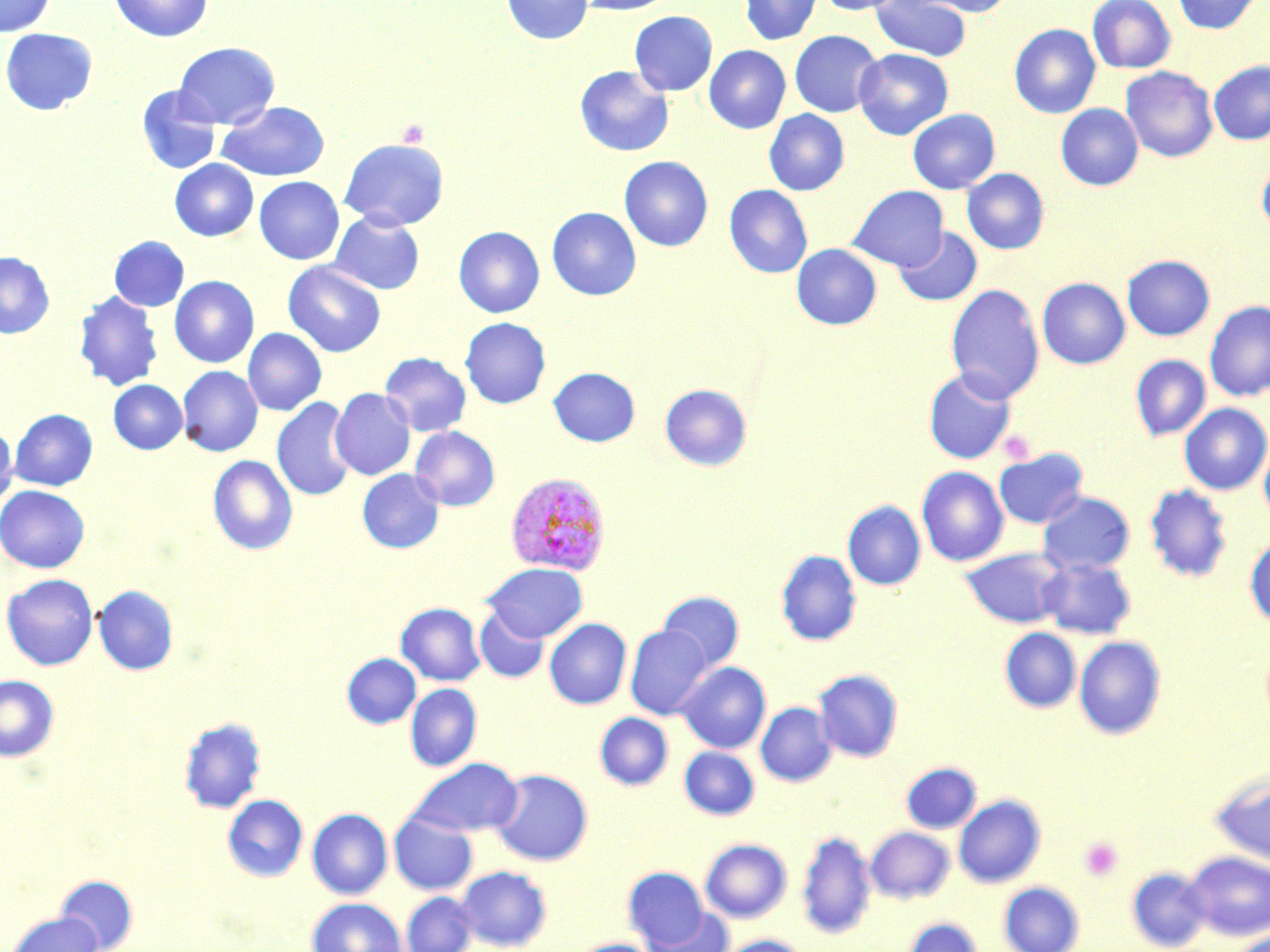

Approximate bounding boxes as (x1,y1)-(x2,y2) corner pairs in pixels. Plasmodium vivax-infected red blood cell locations: (505,471)-(611,576). Uninfected red blood cell locations: (0,0)-(55,36), (108,0)-(214,42), (501,0)-(593,45), (574,0)-(676,15), (740,0)-(821,45), (815,0)-(906,15), (871,0)-(972,61), (913,0)-(1016,16), (1088,0)-(1175,73), (1173,0)-(1260,34), (629,11)-(717,96), (1009,24)-(1100,118), (0,28)-(98,115), (789,30)-(883,117), (173,42)-(280,129), (704,45)-(791,133), (853,48)-(953,139), (1209,59)-(1270,145), (575,65)-(673,156), (1121,66)-(1218,162), (136,86)-(221,174), (217,101)-(330,181), (1056,103)-(1143,190), (764,109)-(849,195), (908,109)-(999,193), (340,138)-(449,230), (619,156)-(713,251), (1257,158)-(1270,237), (170,159)-(258,241), (962,168)-(1049,254), (254,176)-(344,264), (724,184)-(812,278), (848,185)-(948,271), (547,207)-(641,300), (329,211)-(425,295), (453,226)-(544,318), (894,227)-(982,306), (109,236)-(189,311), (791,244)-(882,329), (0,252)-(54,338), (1122,255)-(1215,341), (282,261)-(386,357), (170,276)-(258,367), (1037,277)-(1130,369), (946,284)-(1044,402), (74,291)-(163,391), (1204,300)-(1270,401), (460,317)-(551,408), (243,328)-(326,416), (380,352)-(472,437), (1130,354)-(1211,441), (178,365)-(263,456), (549,367)-(639,446), (924,367)-(1018,464), (109,380)-(188,454), (660,384)-(752,471), (330,388)-(416,480), (272,397)-(357,501), (1180,403)-(1270,494), (10,409)-(97,490), (0,426)-(18,510), (410,426)-(500,511), (1259,435)-(1270,526), (994,448)-(1088,528), (207,455)-(298,555), (916,466)-(1008,566), (357,468)-(445,553), (1144,484)-(1232,582), (0,485)-(89,572), (1037,491)-(1135,575), (843,500)-(925,590), (1245,537)-(1270,627), (960,548)-(1068,628), (776,550)-(861,646), (1038,557)-(1137,639), (482,563)-(588,642), (1,573)-(99,671), (93,585)-(178,675), (658,591)-(744,672), (396,602)-(485,685), (474,607)-(549,683), (544,618)-(632,709), (625,625)-(713,720), (1000,628)-(1081,713), (1074,636)-(1166,740), (342,653)-(420,729), (677,662)-(771,753), (814,669)-(903,762), (0,675)-(59,761), (406,684)-(481,771), (756,702)-(837,786), (594,712)-(673,790), (178,716)-(267,814), (680,746)-(759,819), (408,758)-(523,837), (901,762)-(981,833), (491,769)-(593,865), (1208,770)-(1270,868), (222,794)-(308,882), (953,795)-(1046,888), (307,808)-(393,898), (389,812)-(477,896), (866,826)-(954,903), (796,829)-(875,939), (700,839)-(792,922), (1184,851)-(1270,940), (455,865)-(552,951), (1127,866)-(1211,951), (623,867)-(710,949), (54,874)-(138,951), (998,881)-(1085,952), (401,891)-(479,952), (307,898)-(407,952), (646,909)-(733,952), (4,911)-(105,952), (901,917)-(983,952), (1230,929)-(1270,952), (717,935)-(810,952), (572,938)-(658,952). Platelet locations: (396,119)-(429,148), (998,429)-(1035,464), (1079,836)-(1123,882). Slide-level diagnosis: Plasmodium vivax. Image is 1270×952 pixels. One field of a larger specimen. Optical microscopy. May-Grünwald-Giemsa-stained preparation. 1000x magnification. Thin blood smear.